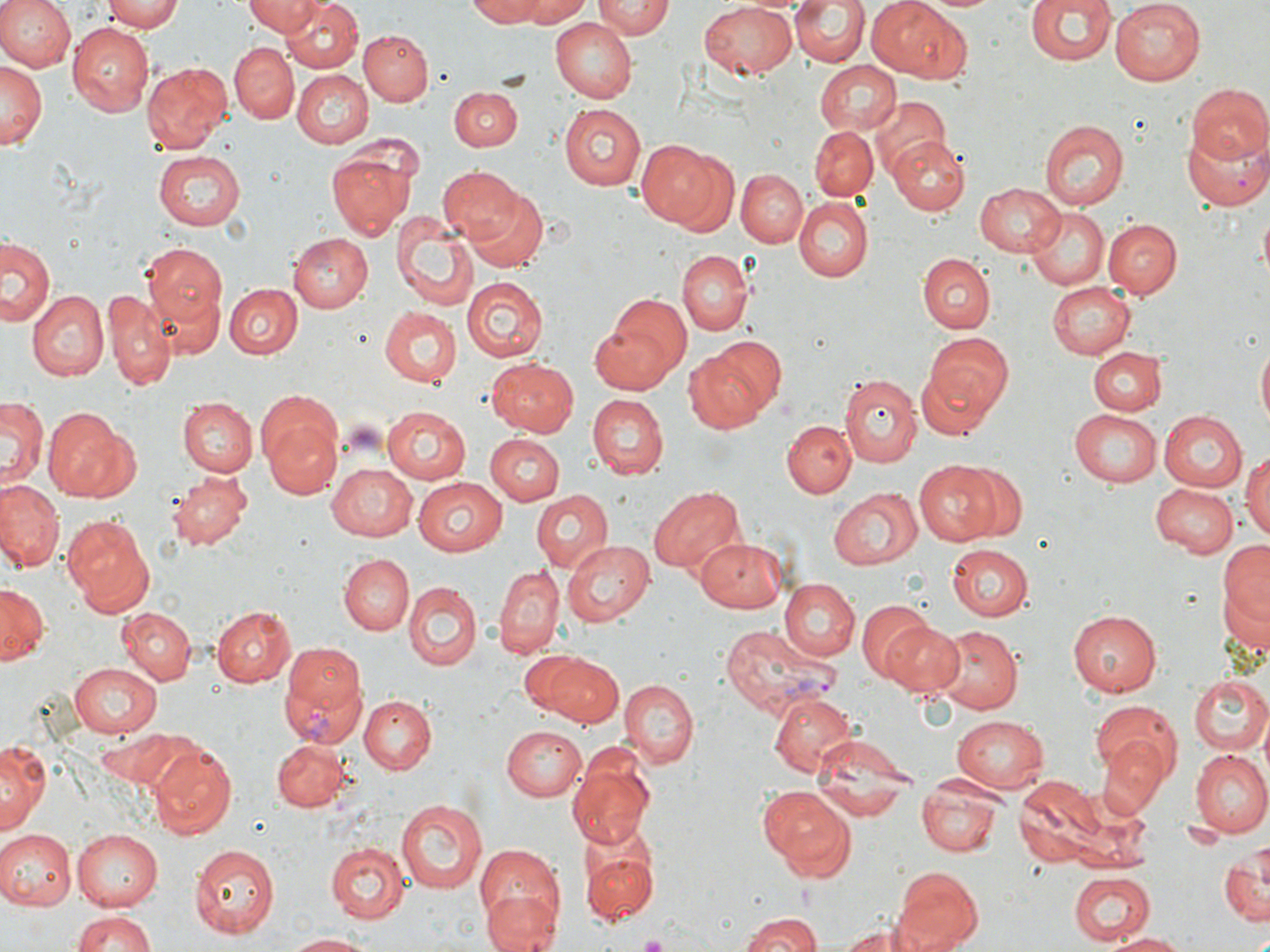

Approximate bounding boxes as (x1, y1, x2, y2) in pixels. Uninfected red blood cell locations: (0, 0, 75, 73), (105, 0, 184, 32), (245, 0, 322, 36), (463, 0, 548, 26), (512, 0, 595, 26), (597, 0, 672, 40), (864, 0, 969, 83), (921, 0, 1001, 14), (1024, 0, 1116, 67), (1111, 0, 1206, 86), (281, 1, 363, 73), (699, 1, 798, 78), (792, 1, 868, 67), (550, 16, 637, 103), (68, 22, 155, 116), (360, 30, 432, 105), (230, 42, 297, 123), (816, 59, 903, 138), (0, 60, 44, 151), (143, 62, 230, 154), (292, 70, 370, 148), (1186, 84, 1270, 166), (451, 86, 521, 152), (870, 97, 951, 181), (560, 103, 648, 190), (1040, 120, 1128, 212), (1182, 120, 1269, 212), (810, 125, 878, 202), (887, 136, 969, 214), (637, 139, 734, 231), (327, 146, 417, 240), (152, 149, 246, 231), (438, 166, 525, 243), (736, 169, 808, 246), (462, 182, 550, 269), (975, 182, 1066, 257), (793, 199, 871, 280), (1022, 205, 1108, 291), (1258, 210, 1269, 283), (390, 211, 478, 311), (1103, 219, 1182, 298), (288, 234, 372, 314), (1, 240, 54, 329), (140, 240, 226, 334), (679, 249, 752, 335), (918, 254, 995, 332), (462, 277, 547, 361), (1047, 279, 1136, 359), (225, 284, 302, 359), (29, 292, 108, 380), (595, 292, 692, 388), (105, 293, 176, 389), (379, 305, 461, 385), (924, 334, 1013, 417), (689, 339, 783, 430), (1256, 341, 1269, 434), (1087, 347, 1166, 416), (487, 357, 580, 435), (916, 364, 1001, 441), (840, 375, 921, 469), (586, 395, 667, 479), (177, 397, 256, 477), (0, 398, 46, 490), (259, 403, 342, 498), (382, 406, 472, 484), (42, 407, 135, 501), (1070, 409, 1162, 487), (1157, 410, 1246, 494), (782, 419, 855, 498), (486, 432, 565, 503), (1242, 450, 1270, 542), (913, 461, 1003, 544), (327, 462, 418, 539), (959, 463, 1027, 538), (168, 471, 251, 548), (414, 476, 511, 555), (0, 480, 64, 571), (1151, 484, 1237, 557), (647, 485, 745, 576), (831, 487, 921, 569), (530, 488, 612, 575), (61, 514, 156, 613), (694, 536, 788, 612), (1217, 537, 1269, 647), (561, 538, 655, 626), (946, 542, 1033, 620), (338, 553, 413, 634), (494, 564, 562, 659), (778, 580, 858, 660), (404, 581, 481, 672), (0, 583, 49, 663), (857, 600, 938, 683), (213, 605, 297, 687), (119, 608, 194, 682), (1068, 611, 1161, 696), (882, 622, 964, 696), (931, 623, 1024, 711), (548, 656, 622, 727), (70, 661, 163, 735), (1187, 674, 1270, 752), (619, 679, 699, 769), (768, 689, 859, 778), (359, 695, 435, 773), (1090, 702, 1182, 782), (953, 714, 1054, 788), (502, 725, 586, 801), (812, 736, 917, 806), (272, 737, 348, 810), (1095, 739, 1168, 818), (0, 742, 48, 832), (149, 744, 238, 837), (1189, 748, 1270, 837), (567, 759, 655, 847), (1013, 776, 1103, 866), (917, 780, 1003, 854), (757, 787, 856, 881), (395, 799, 488, 895), (72, 827, 163, 910), (0, 828, 75, 911), (326, 840, 411, 923), (187, 841, 279, 937), (581, 841, 658, 925), (1222, 844, 1269, 927), (472, 846, 564, 942), (890, 867, 985, 952), (1068, 872, 1155, 945), (482, 886, 559, 952), (69, 911, 157, 951), (739, 915, 825, 951), (838, 919, 929, 952), (1108, 931, 1190, 951), (284, 932, 376, 951). Plasmodium vivax-infected red blood cell locations: (720, 624, 829, 717), (280, 642, 367, 742). Slide-level diagnosis: Plasmodium vivax. One field of a larger specimen. Thin blood smear. Image is 1270×952 pixels. Captured at 1000x magnification. May-Grünwald-Giemsa-stained preparation. Optical microscopy.